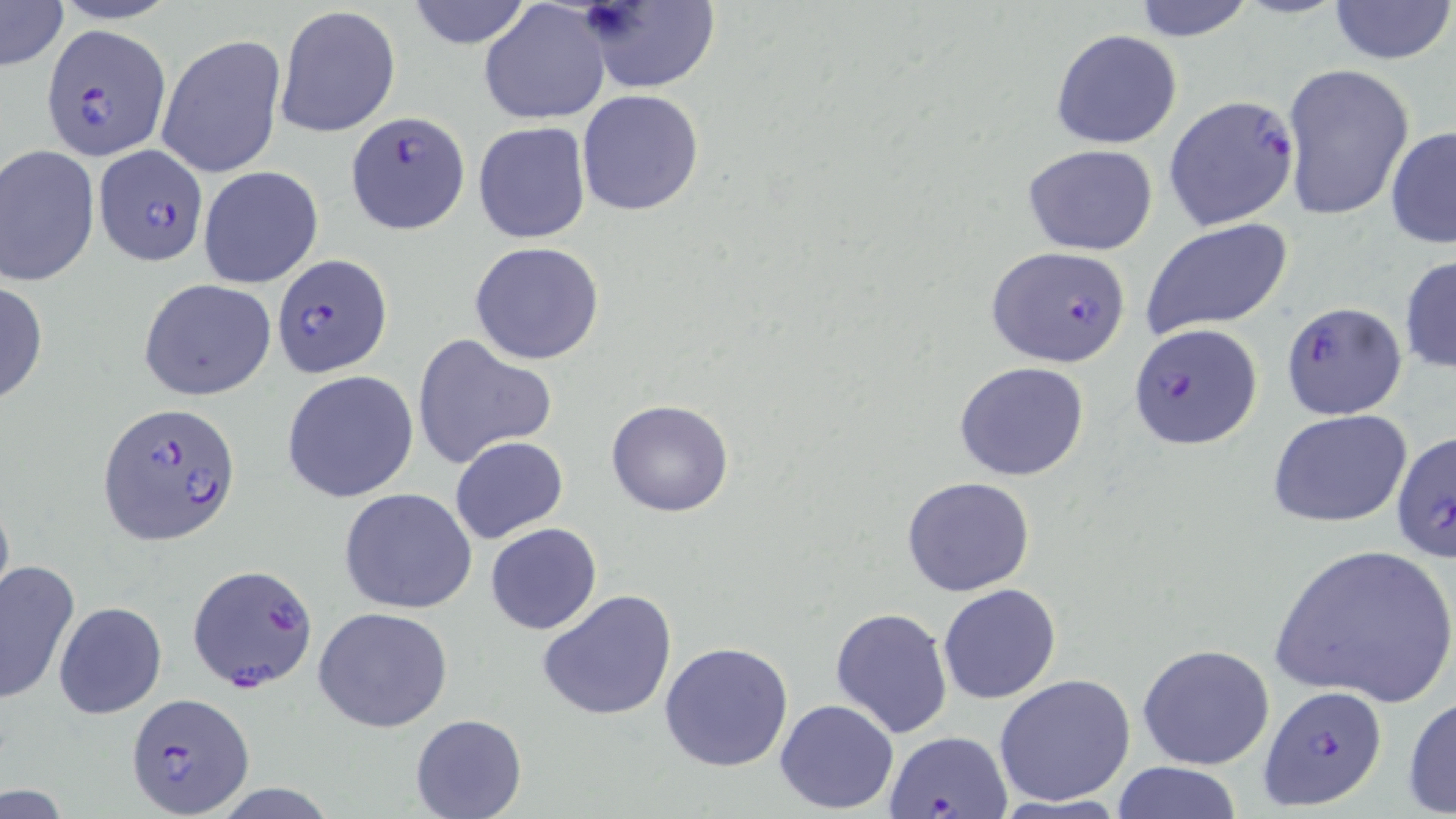

Approximate bounding boxes as (x1,y1)-(x2,y2) corner pairs in pixels. Plasmodium falciparum-infected red blood cell locations: (40,24)-(171,159), (1164,95)-(1301,233), (346,110)-(471,235), (95,143)-(205,268), (989,243)-(1131,367), (272,254)-(393,377), (1281,300)-(1407,421), (1128,322)-(1262,449), (98,400)-(242,546), (1391,430)-(1456,563), (187,563)-(320,693), (1257,685)-(1389,810), (127,693)-(255,818), (883,732)-(1014,818). Uninfected red blood cell locations: (1,0)-(68,71), (406,0)-(532,49), (1128,0)-(1257,42), (1325,0)-(1454,67), (577,2)-(720,93), (479,3)-(610,126), (274,5)-(402,139), (1050,28)-(1184,149), (157,33)-(287,180), (1281,63)-(1415,222), (576,90)-(705,215), (472,120)-(592,244), (1385,125)-(1456,248), (0,144)-(100,291), (1024,144)-(1160,256), (198,165)-(323,288), (1140,218)-(1295,335), (469,241)-(606,365), (1399,253)-(1455,376), (139,277)-(277,401), (0,278)-(49,408), (411,334)-(557,470), (954,362)-(1091,481), (281,370)-(421,503), (606,399)-(734,518), (1267,409)-(1412,527), (450,435)-(569,545), (901,475)-(1037,597), (338,487)-(478,614), (0,494)-(15,616), (485,522)-(602,635), (1268,542)-(1456,708), (0,560)-(79,706), (938,583)-(1061,705), (537,589)-(678,722), (54,601)-(167,719), (313,606)-(454,733), (830,606)-(954,739), (659,639)-(795,773), (1137,643)-(1276,771), (993,675)-(1138,807), (1403,694)-(1455,817), (775,698)-(899,815), (410,714)-(526,819), (1110,761)-(1243,818). Slide-level diagnosis: Plasmodium falciparum. Image is 1456×819 pixels. Thin blood smear. Single field of view. 1000x magnification. May-Grünwald-Giemsa stain. Optical microscopy.